Outline each uninfected red blood cell.
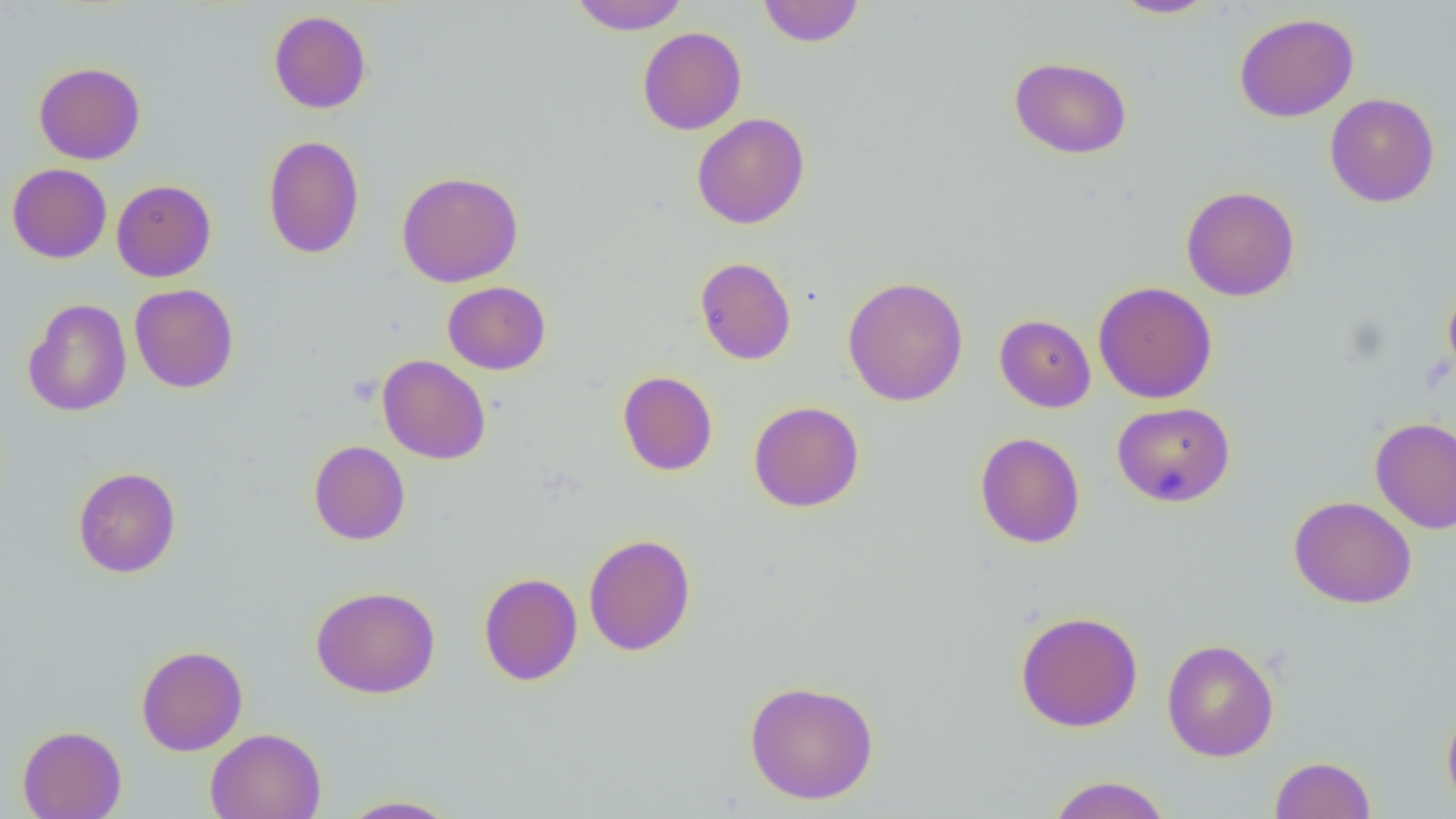
Approximate bounding boxes as (x1, y1, x2, y2) in pixels.
Uninfected red blood cells: (570, 0, 690, 35), (757, 0, 865, 47), (1109, 0, 1218, 18), (268, 9, 372, 114), (1233, 12, 1359, 122), (637, 27, 747, 135), (1008, 56, 1132, 159), (33, 62, 145, 165), (1325, 92, 1440, 207), (692, 113, 809, 230), (263, 134, 364, 259), (7, 163, 112, 263), (396, 170, 523, 287), (111, 179, 216, 282), (1181, 186, 1300, 301), (695, 257, 797, 365), (842, 276, 969, 406), (442, 281, 551, 375), (1093, 281, 1218, 403), (1443, 281, 1456, 382), (129, 283, 239, 393), (23, 299, 132, 417), (994, 314, 1096, 413), (378, 355, 490, 465), (617, 370, 718, 476), (748, 401, 865, 512), (1112, 401, 1235, 507), (1370, 417, 1456, 533), (974, 431, 1086, 549), (308, 440, 410, 545), (72, 466, 181, 578), (1289, 495, 1417, 609), (583, 533, 696, 656), (478, 572, 582, 686), (311, 585, 440, 699), (1015, 610, 1144, 732), (1162, 638, 1279, 762), (136, 644, 248, 756), (743, 679, 879, 804), (1441, 700, 1456, 815), (17, 725, 127, 819), (205, 728, 325, 819), (1270, 756, 1376, 819), (1046, 775, 1172, 819), (338, 794, 461, 818).

Slide-level diagnosis: no evidence of blood parasites. Thin blood film. One field of a larger specimen. 1000x magnification. Image is 1456×819 pixels. Optical microscopy.